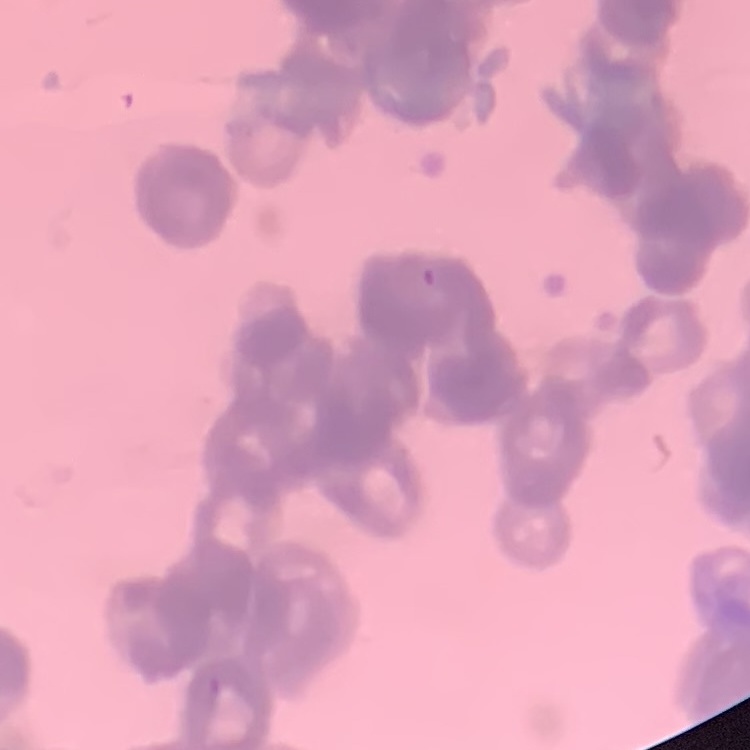

The red blood cells exhibit rouleaux formation. Square crop of a larger photomicrograph. Thin peripheral smear. Stained with either Field's or Giemsa.